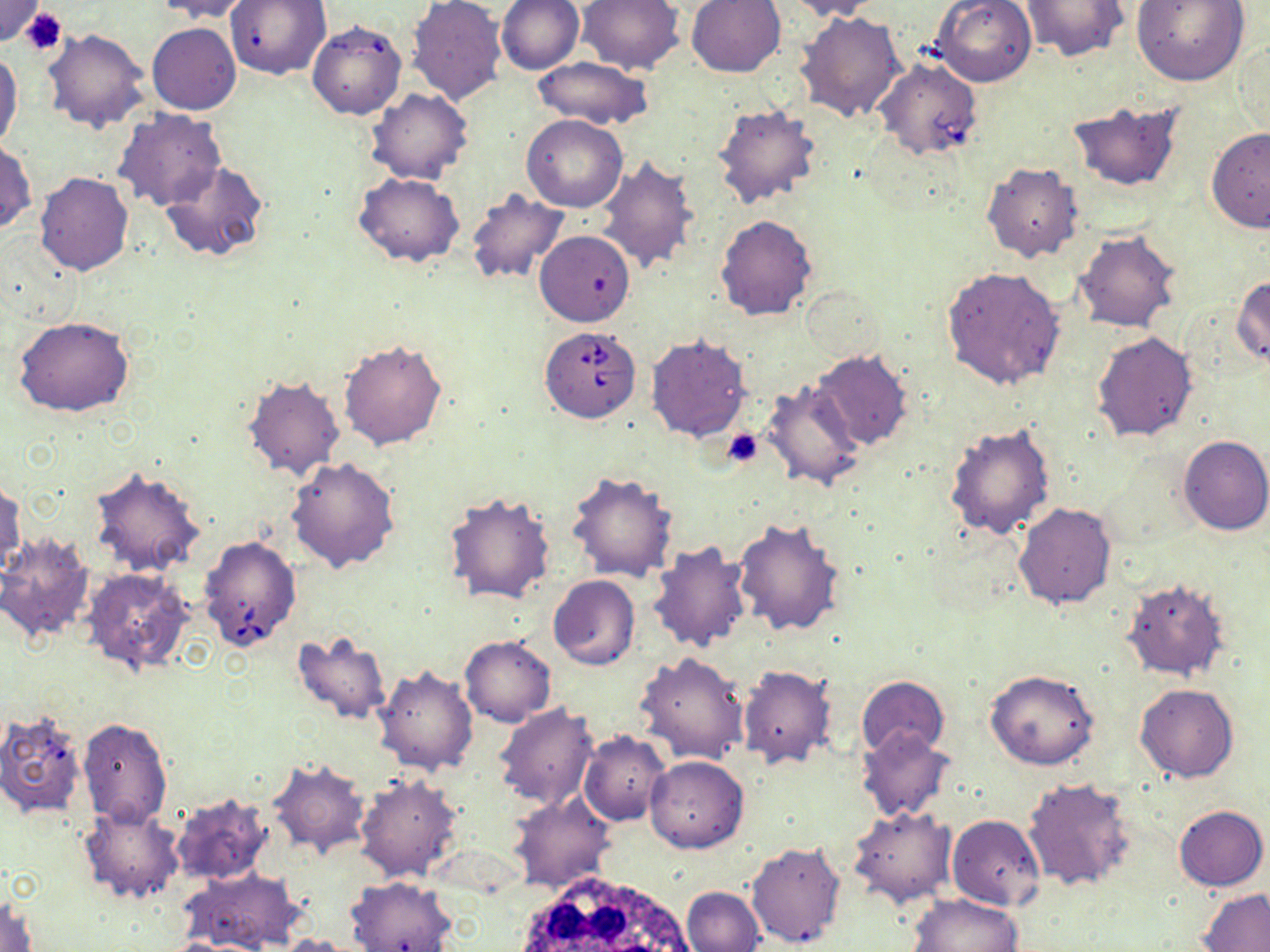 Approximate bounding boxes as (x1, y1, x2, y2) in pixels. White blood cell locations: (505, 872, 703, 952). Uninfected red blood cell locations: (151, 0, 254, 23), (226, 0, 331, 79), (407, 0, 505, 105), (496, 0, 584, 75), (576, 0, 685, 75), (687, 0, 785, 77), (783, 0, 885, 21), (1133, 0, 1249, 85), (0, 1, 45, 47), (931, 1, 1037, 86), (1020, 1, 1126, 62), (796, 11, 907, 123), (307, 19, 406, 120), (147, 22, 241, 115), (42, 28, 150, 133), (1233, 35, 1268, 136), (0, 48, 23, 155), (532, 57, 655, 129), (367, 88, 473, 185), (1067, 99, 1186, 195), (711, 103, 823, 209), (114, 109, 226, 213), (522, 115, 628, 211), (1205, 127, 1270, 232), (0, 140, 35, 236), (594, 155, 698, 274), (159, 160, 269, 265), (982, 163, 1084, 263), (34, 172, 133, 277), (353, 173, 463, 265), (465, 190, 569, 286), (715, 214, 817, 319), (535, 230, 634, 326), (1072, 230, 1181, 332), (940, 265, 1068, 389), (1233, 275, 1270, 369), (12, 316, 135, 417), (1090, 331, 1199, 443), (645, 333, 753, 442), (339, 337, 448, 449), (810, 350, 913, 451), (242, 373, 345, 479), (759, 379, 866, 491), (944, 423, 1057, 540), (1177, 435, 1269, 536), (285, 456, 401, 574), (88, 465, 206, 577), (566, 470, 679, 583), (0, 480, 26, 580), (444, 491, 557, 606), (1012, 502, 1117, 610), (732, 519, 846, 638), (0, 531, 96, 645), (648, 539, 752, 651), (82, 568, 194, 677), (549, 575, 640, 670), (1121, 579, 1229, 681), (291, 630, 391, 725), (460, 635, 556, 726), (635, 651, 749, 765), (373, 664, 477, 777), (737, 665, 837, 769), (985, 669, 1099, 770), (856, 675, 948, 759), (1135, 683, 1240, 783), (494, 704, 599, 809), (0, 710, 87, 818), (77, 717, 173, 827), (857, 727, 955, 821), (579, 730, 671, 826), (644, 756, 749, 853), (265, 757, 371, 860), (353, 775, 463, 884), (1023, 776, 1136, 894), (170, 792, 274, 886), (509, 793, 617, 894), (78, 802, 185, 904), (1172, 805, 1267, 891), (848, 806, 957, 908), (947, 813, 1045, 910), (746, 840, 848, 949), (183, 867, 301, 952), (346, 876, 459, 952), (682, 886, 764, 952), (1198, 888, 1270, 951), (908, 893, 1024, 952), (1, 894, 40, 952), (272, 934, 354, 952). Babesia divergens-infected red blood cell locations: (873, 57, 983, 160), (540, 326, 640, 423), (198, 534, 301, 653). Platelet locations: (20, 7, 67, 56), (723, 428, 763, 467). Slide-level diagnosis: Babesia divergens. Captured at 1000x magnification. Image is 1270×952 pixels. Light microscopy. One field of a larger specimen. Thin blood smear. May-Grünwald-Giemsa stain.